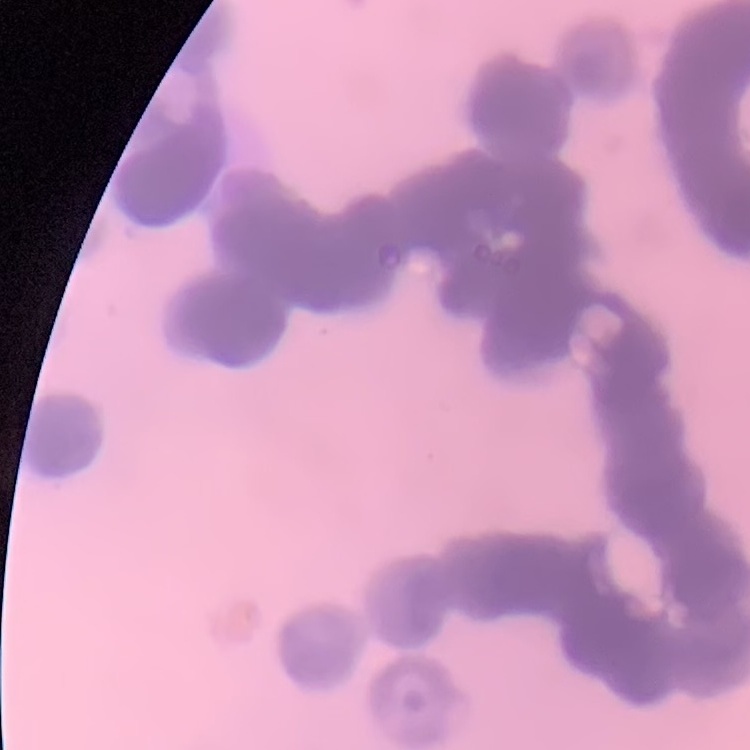

red blood cell morphology = rouleaux formation
preparation = thin blood film
stain = Field's or Giemsa
image type = one tile cut from a larger photomicrograph